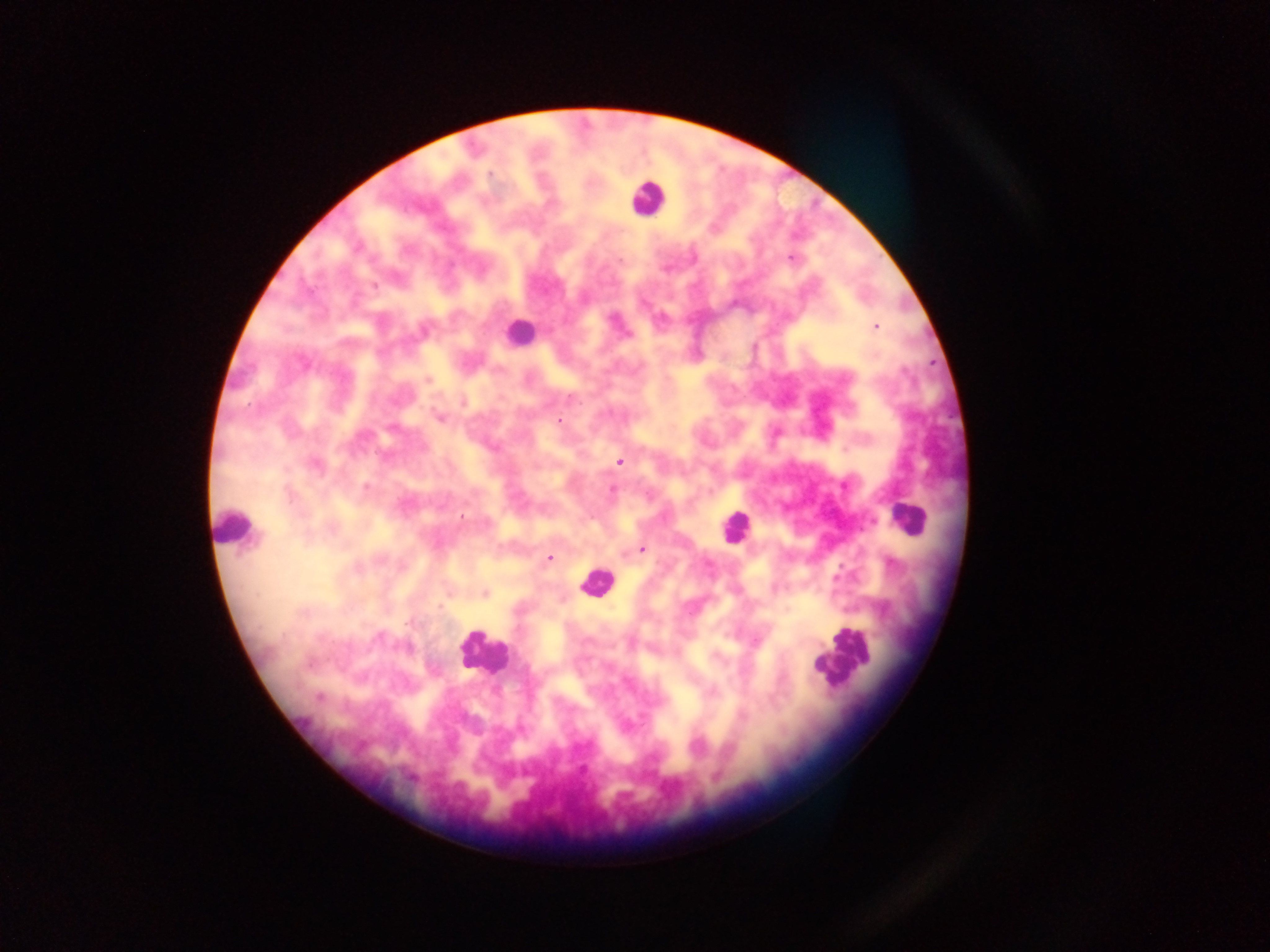
Approximate centers as {x, y} in pixels. Plasmodium parasite locations: {490, 174}, {791, 257}, {875, 326}, {427, 379}, {440, 416}, {558, 420}, {619, 461}, {314, 464}, {613, 491}, {640, 549}, {549, 557}, {484, 593}. Leukocyte locations: {645, 197}, {519, 332}, {908, 519}, {233, 529}, {734, 529}, {597, 581}, {481, 651}, {841, 659}. Mobile-phone photograph taken through the microscope. Image is 1270×952 pixels. Thick blood smear. Collected in Ghana. Single field of view.